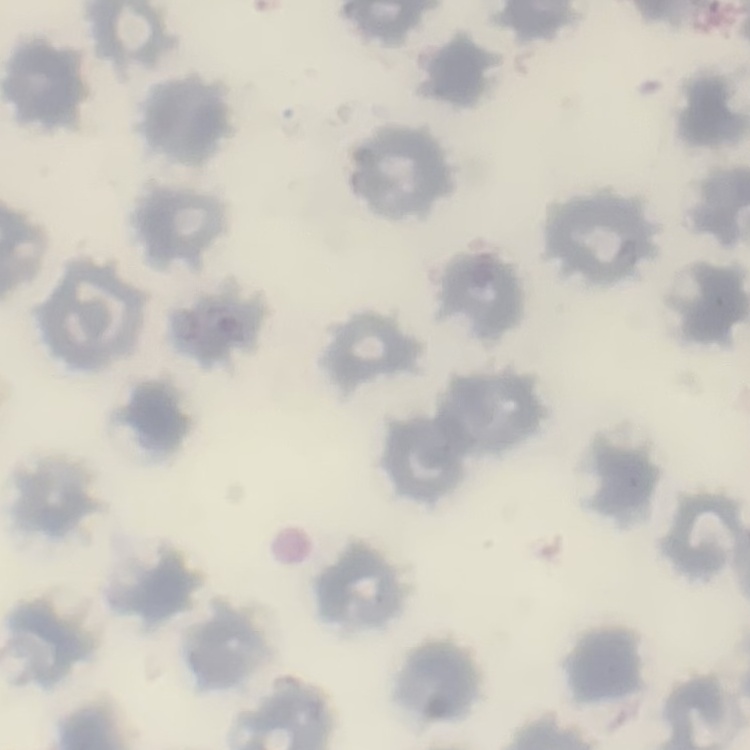

Summary:
  - Erythrocyte morphology: no rouleaux formation
  - Image type: one tile cut from a larger photomicrograph
  - Stain: Field's or Giemsa
  - Preparation: thin peripheral smear